Identify the blood parasite species.
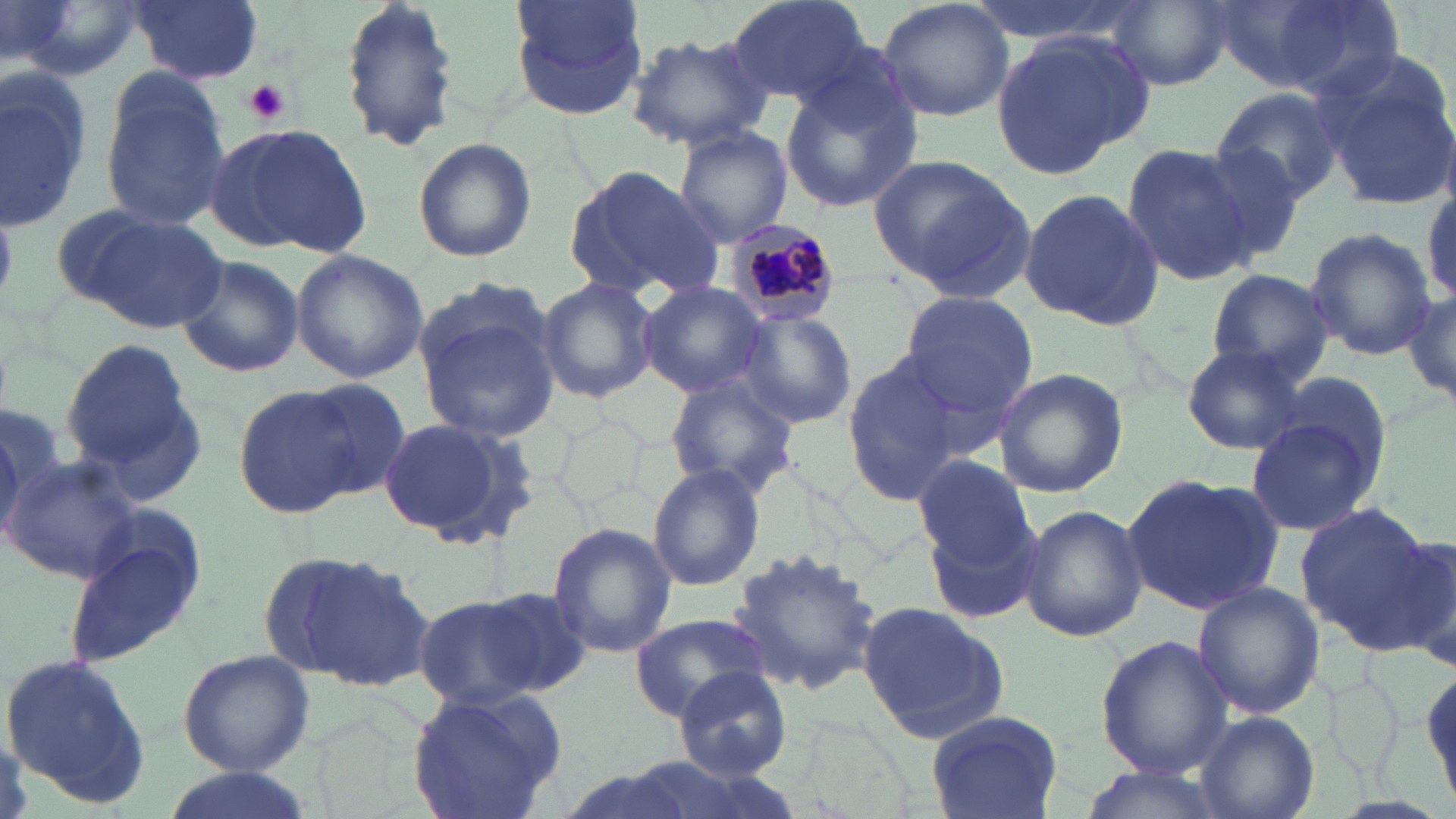

Plasmodium malariae.

Approximate bounding boxes as (x1, y1, x2, y2) in pixels. Uninfected red blood cell locations: (14, 0, 145, 81), (129, 0, 263, 83), (337, 0, 462, 155), (507, 0, 647, 122), (726, 0, 878, 108), (878, 0, 1015, 122), (965, 0, 1146, 45), (1, 1, 79, 72), (1107, 1, 1238, 89), (1209, 2, 1389, 95), (625, 33, 773, 150), (991, 33, 1149, 179), (1316, 54, 1456, 210), (1, 70, 93, 232), (778, 71, 922, 215), (1212, 85, 1345, 203), (99, 87, 229, 231), (215, 124, 373, 257), (673, 127, 794, 246), (1192, 135, 1310, 267), (412, 137, 538, 262), (1120, 142, 1261, 288), (870, 155, 1035, 297), (565, 164, 726, 303), (1018, 187, 1167, 329), (67, 207, 228, 335), (1304, 228, 1435, 359), (289, 249, 429, 383), (174, 253, 303, 381), (1206, 267, 1335, 385), (536, 276, 659, 402), (636, 281, 770, 398), (1403, 285, 1456, 410), (895, 289, 1039, 430), (414, 291, 561, 442), (736, 310, 856, 427), (61, 338, 193, 467), (1182, 344, 1307, 455), (840, 352, 967, 504), (991, 367, 1129, 499), (663, 373, 802, 496), (75, 379, 213, 503), (297, 381, 411, 497), (233, 383, 366, 519), (1, 398, 62, 545), (1243, 413, 1384, 536), (374, 414, 539, 544), (911, 453, 1035, 569), (4, 456, 144, 589), (648, 463, 765, 590), (1120, 471, 1284, 619), (923, 499, 1049, 630), (1021, 503, 1145, 642), (1294, 505, 1437, 650), (548, 523, 675, 658), (1372, 528, 1456, 668), (62, 531, 205, 672), (726, 547, 884, 692), (275, 550, 433, 689), (1192, 580, 1324, 721), (479, 588, 594, 696), (418, 595, 547, 713), (856, 601, 1012, 743), (631, 615, 770, 720), (1094, 634, 1232, 778), (176, 649, 314, 776), (2, 654, 155, 809), (1420, 664, 1453, 810), (675, 667, 792, 780), (1329, 674, 1402, 785), (404, 686, 565, 819), (925, 707, 1061, 817), (1194, 711, 1319, 819), (551, 765, 700, 819), (1075, 765, 1228, 818), (155, 768, 320, 819). Plasmodium malariae-infected red blood cell locations: (723, 218, 842, 328). Platelet locations: (241, 79, 292, 124). Image is 1456×819 pixels. Light microscopy. Captured at 1000x magnification. May-Grünwald-Giemsa-stained preparation. Thin blood smear. One field of a larger specimen.